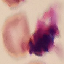

Malaria status: uninfected. Thin smear of blood. Photographed with a smartphone camera at the microscope eyepiece. Cell patch, automatically extracted from a larger field of view and resized to 64 × 64 pixels. Giemsa stain.